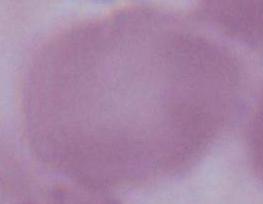
Summary:
  - Magnification: 1000x
  - Modality: micrograph
  - Identification: red blood cell